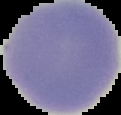
{
  "image_type": "segmented cell region with the area outside set to black",
  "preparation": "thin blood film",
  "image_size": "121×115 pixels",
  "result": "no malaria parasites seen"
}